Assess the morphology of the erythrocytes.
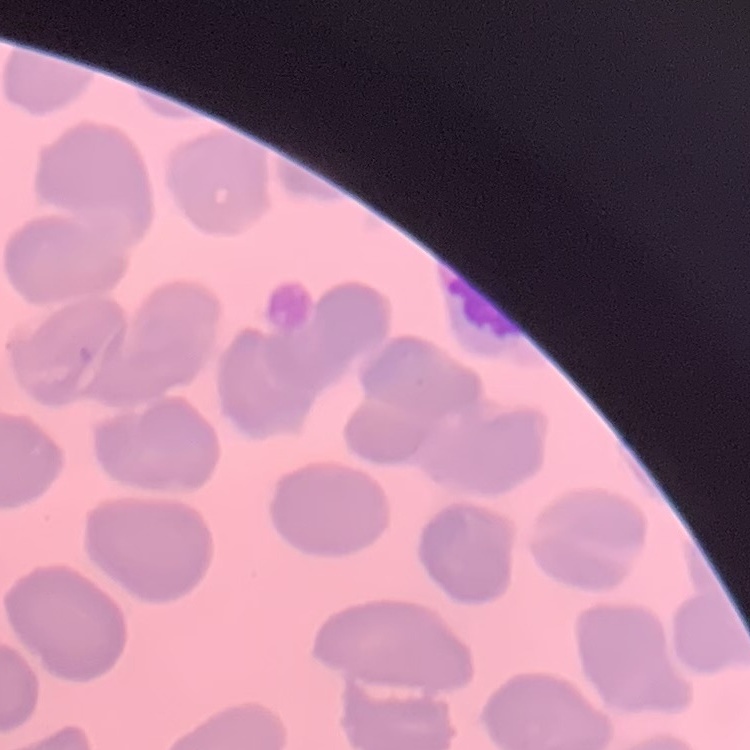

They show no rouleaux formation.

Summary:
  - Preparation: thin blood film
  - Image type: one tile cut from a larger photomicrograph
  - Stain: Field's or Giemsa